Identify the preparation type.
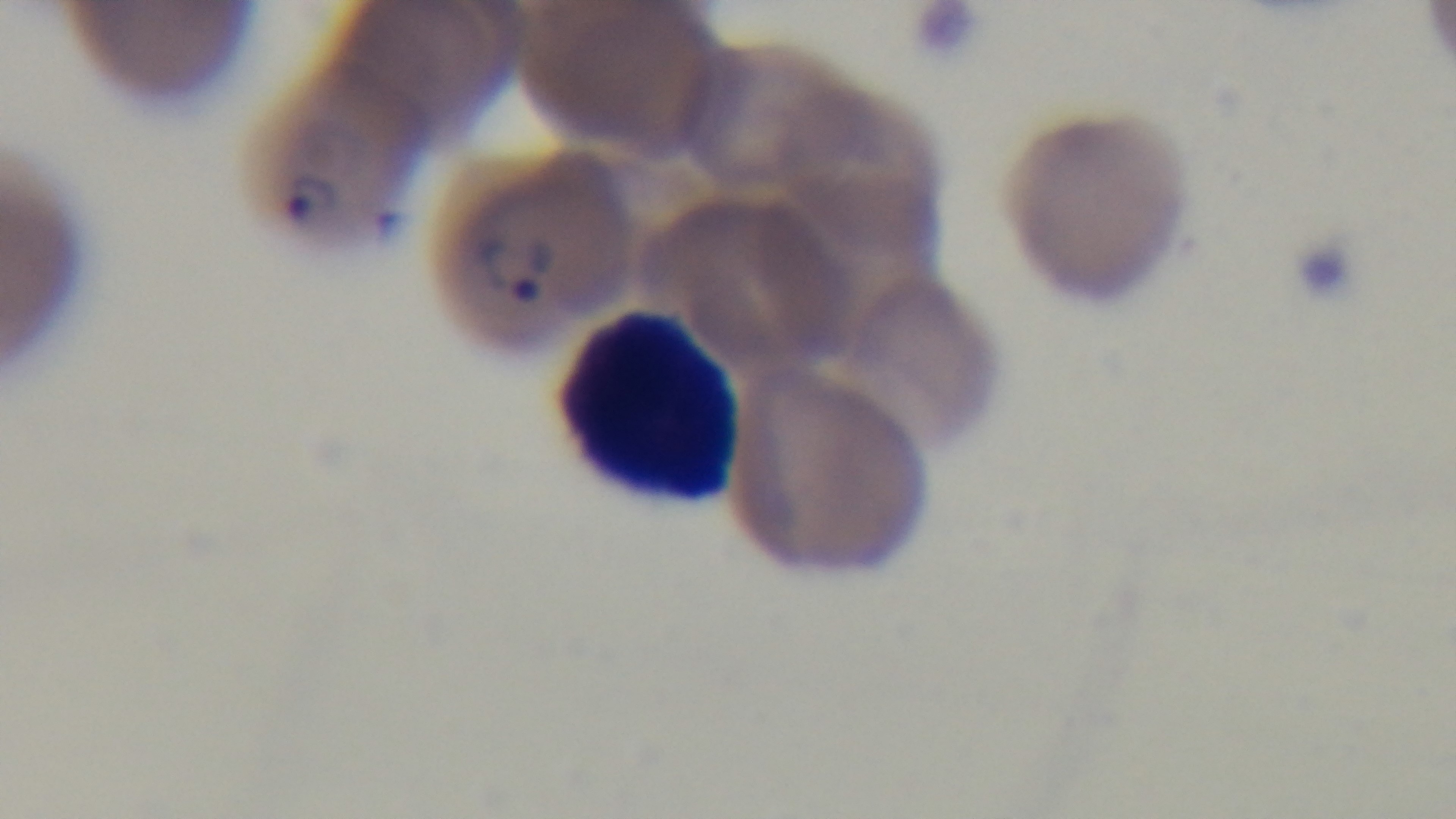

Thin.

field of view = single
capture = mounted 4K digital camera
malaria status = infected
modality = light microscopy
stain = Giemsa
objective = 100x oil immersion